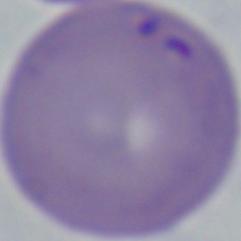
identification: Babesia
modality: micrograph
magnification: 1000x